Describe the morphology of the erythrocytes.
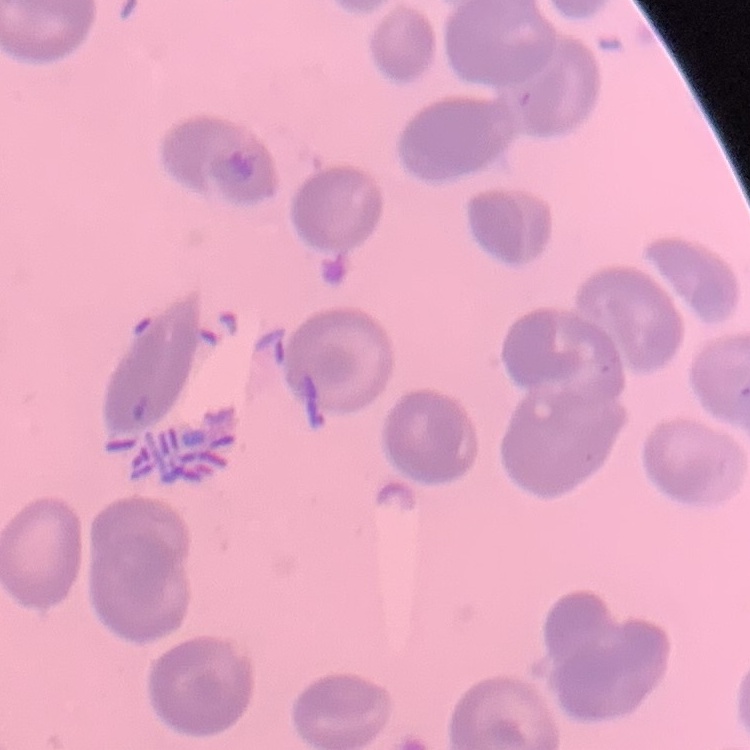
No rouleaux formation.

stain = Field's or Giemsa
image type = one tile cut from a larger photomicrograph
preparation = thin peripheral smear